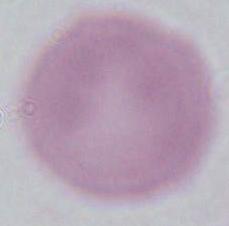
modality = micrograph
identification = red blood cell
magnification = 1000x